Point out each malaria parasite.
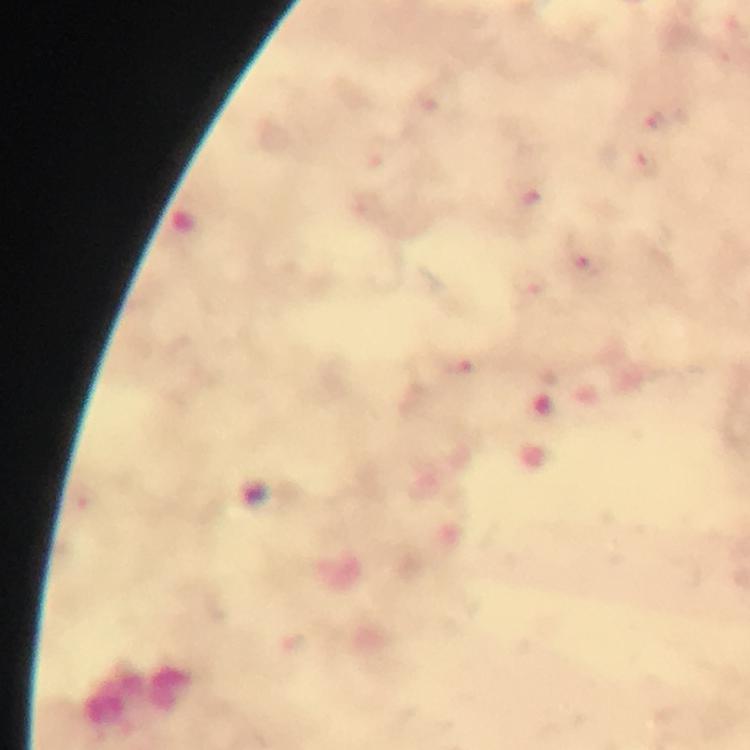

Approximate object centers, in pixels from the top-left corner.
Malaria parasites: (x=656, y=122), (x=648, y=164), (x=591, y=263), (x=533, y=285), (x=457, y=368).

immersion oil = used
context = from a malaria diagnostic workup
cropped from = one field of view
preparation = thick blood smear
capture = smartphone mounted on the microscope
stain = Giemsa
magnification = 100x
image size = 750×750 pixels